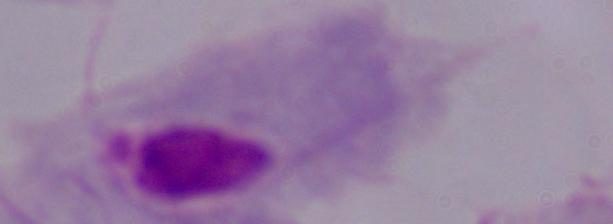
Summary:
  - Modality: micrograph
  - Magnification: 1000x
  - Identification: trichomonad